Name the parasite shown.
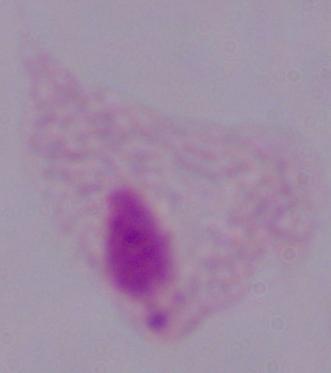
This is a trichomonad.

Summary:
  - Modality: micrograph
  - Magnification: 1000x